State which cell type is depicted.
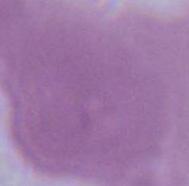
An erythrocyte.

Summary:
  - Magnification: 1000x
  - Modality: micrograph